Comment on the morphology of the red blood cells.
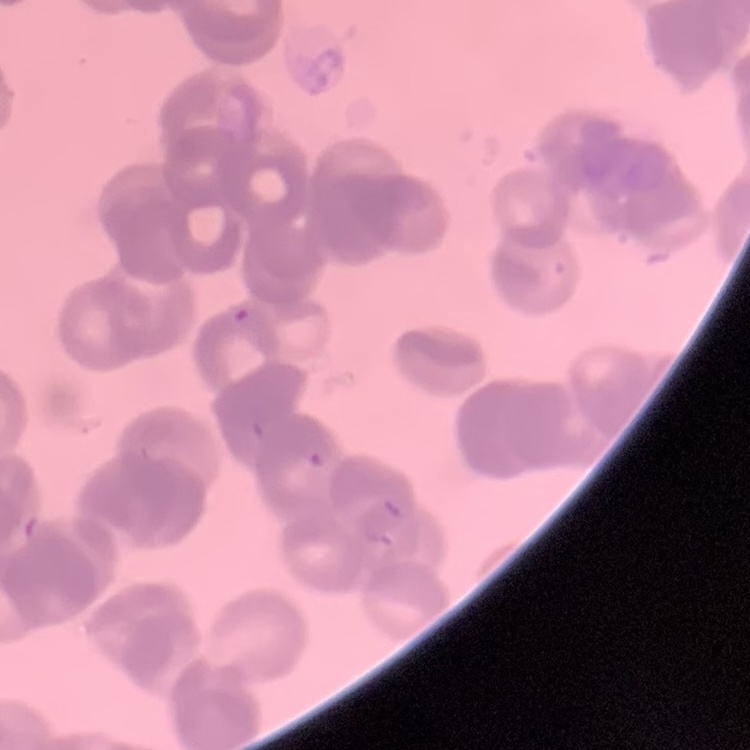

They show rouleaux formation.

Thin blood film. One tile cut from a larger photomicrograph. Stained with either Field's or Giemsa.